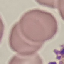

result = no malaria parasites detected
capture = smartphone camera at the microscope eyepiece
stain = Giemsa
image type = automatically extracted cell patch, resized to 64 × 64 pixels
preparation = thin blood film